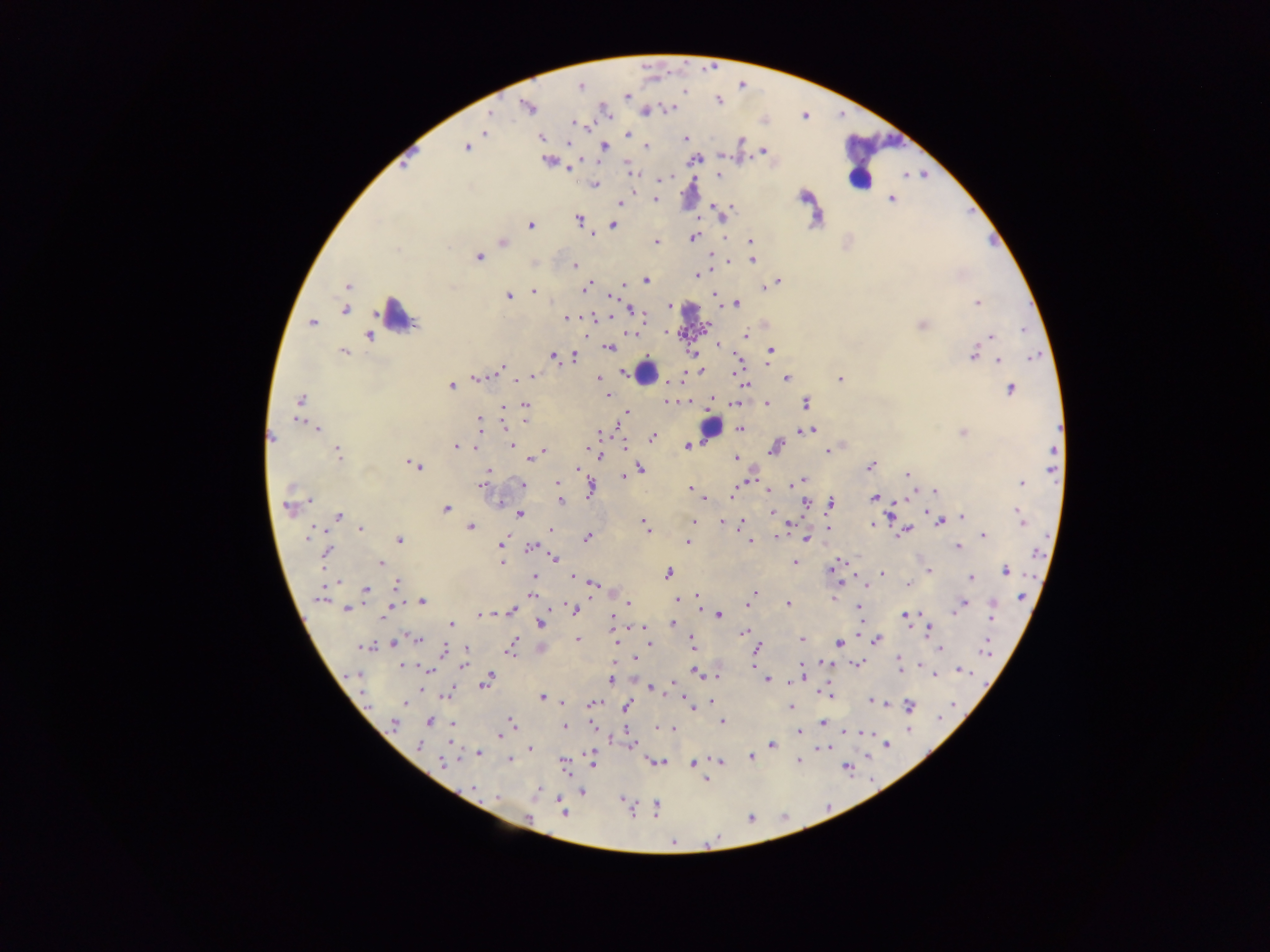

Approximate centers as {x, y} in pixels.
Summary:
  - Plasmodium parasite locations (subset; some below the resolvable size): {714, 64}, {649, 67}, {744, 84}, {582, 89}, {685, 91}, {626, 96}, {718, 101}, {528, 106}, {668, 108}, {803, 116}, {485, 132}, {628, 134}, {541, 137}, {685, 139}, {741, 141}, {569, 143}, {604, 146}, {647, 147}, {466, 148}, {764, 150}, {696, 159}, {547, 161}, {401, 163}, {570, 168}, {631, 171}, {719, 175}, {923, 175}, {668, 177}, {595, 184}, {803, 196}, {891, 199}, {656, 200}, {621, 203}, {713, 203}, {731, 206}, {696, 216}, {578, 219}, {530, 225}, {614, 225}, {592, 235}, {724, 236}, {693, 237}, {750, 241}, {990, 241}, {503, 242}, {656, 242}, {398, 250}, {479, 257}, {728, 258}, {752, 260}, {574, 266}, {697, 275}, {646, 280}, {777, 282}, {623, 284}, {588, 285}, {347, 287}, {586, 288}, {765, 288}, {534, 291}, {714, 295}, {508, 296}, {613, 296}, {737, 303}, {977, 303}, {670, 306}, {345, 310}, {632, 311}, {605, 317}, {566, 318}, {313, 323}, {921, 325}, {1024, 330}, {746, 335}, {990, 336}, {368, 337}, {718, 345}, {610, 348}, {770, 350}, {344, 352}, {973, 355}, {554, 356}, {574, 357}, {1033, 357}, {999, 359}, {501, 368}, {700, 370}, {532, 377}, {477, 378}, {840, 378}, {598, 379}, {787, 379}, {517, 381}, {745, 385}, {451, 386}, {1011, 389}, {606, 396}, {300, 400}, {667, 401}, {735, 403}, {767, 403}, {806, 403}, {525, 405}, {504, 406}, {626, 412}, {297, 420}, {480, 420}, {618, 424}, {507, 425}, {318, 429}, {740, 429}, {810, 430}, {963, 433}, {652, 437}, {271, 438}, {512, 444}, {624, 445}, {687, 446}, {455, 447}, {774, 448}, {474, 449}, {543, 451}, {827, 451}, {337, 453}, {600, 454}, {1053, 457}, {736, 458}, {530, 460}, {415, 465}, {871, 467}, {579, 468}, {641, 468}, {489, 470}, {907, 474}, {623, 476}, {802, 480}, {557, 483}, {1021, 483}, {523, 484}, {795, 484}, {482, 485}, {590, 488}, {691, 489}, {769, 490}, {733, 492}, {935, 492}, {873, 498}, {310, 500}, {561, 503}, {831, 503}, {806, 504}, {287, 508}, {446, 508}, {771, 513}, {520, 515}, {338, 516}, {1021, 516}, {962, 517}, {694, 521}, {940, 521}, {722, 522}, {644, 524}, {741, 524}, {872, 525}, {471, 527}, {828, 528}, {360, 529}, {550, 530}, {906, 530}, {983, 535}, {777, 536}, {587, 538}, {807, 538}, {400, 540}, {688, 542}, {750, 542}, {502, 545}, {957, 546}, {531, 547}, {325, 553}, {555, 558}, {501, 562}, {795, 562}, {381, 563}, {832, 568}, {929, 571}, {1006, 571}, {667, 573}, {882, 573}, {534, 577}, {573, 577}, {970, 578}, {595, 583}, {397, 585}, {908, 585}, {366, 590}, {755, 592}, {532, 594}, {319, 597}, {697, 597}, {1021, 597}, {680, 600}, {422, 601}, {628, 603}, {787, 603}, {963, 605}, {749, 606}, {860, 606}, {573, 608}, {347, 609}, {512, 610}, {482, 615}, {719, 615}, {386, 616}, {905, 616}, {992, 616}, {613, 619}, {673, 622}, {451, 624}, {540, 624}, {929, 629}, {743, 634}, {415, 639}, {514, 640}, {578, 640}, {801, 640}, {876, 641}, {616, 642}, {393, 643}, {650, 643}, {692, 643}, {838, 643}, {363, 647}, {759, 648}, {510, 649}, {940, 649}, {444, 650}, {466, 650}, {985, 651}, {636, 659}, {802, 665}, {858, 665}, {402, 666}, {463, 666}, {900, 666}, {429, 671}, {694, 671}, {961, 671}, {356, 674}, {934, 675}, {489, 677}, {767, 680}, {611, 681}, {487, 682}, {652, 689}, {826, 694}, {542, 697}, {871, 701}, {561, 702}, {877, 702}, {405, 704}, {592, 704}, {626, 706}, {791, 706}, {910, 706}, {694, 707}, {722, 721}, {430, 722}, {512, 722}, {394, 723}, {823, 723}, {453, 724}, {565, 726}, {661, 728}, {670, 728}, {848, 730}, {799, 732}, {500, 734}, {887, 744}, {771, 745}, {419, 746}, {826, 748}, {530, 749}, {478, 753}, {592, 755}, {751, 757}, {510, 760}, {799, 761}, {442, 762}, {658, 762}, {719, 762}, {592, 763}, {693, 764}, {847, 768}, {704, 779}, {474, 788}, {583, 793}, {497, 797}, {623, 799}, {656, 808}, {563, 811}
  - Leukocyte locations: {858, 175}, {398, 317}, {647, 373}, {709, 427}
  - Image size: 1270×952 pixels
  - Capture: mobile-phone photograph through a microscope
  - Field of view: single
  - Country: Ghana
  - Preparation: thick blood film